Locate and identify every blood parasite.
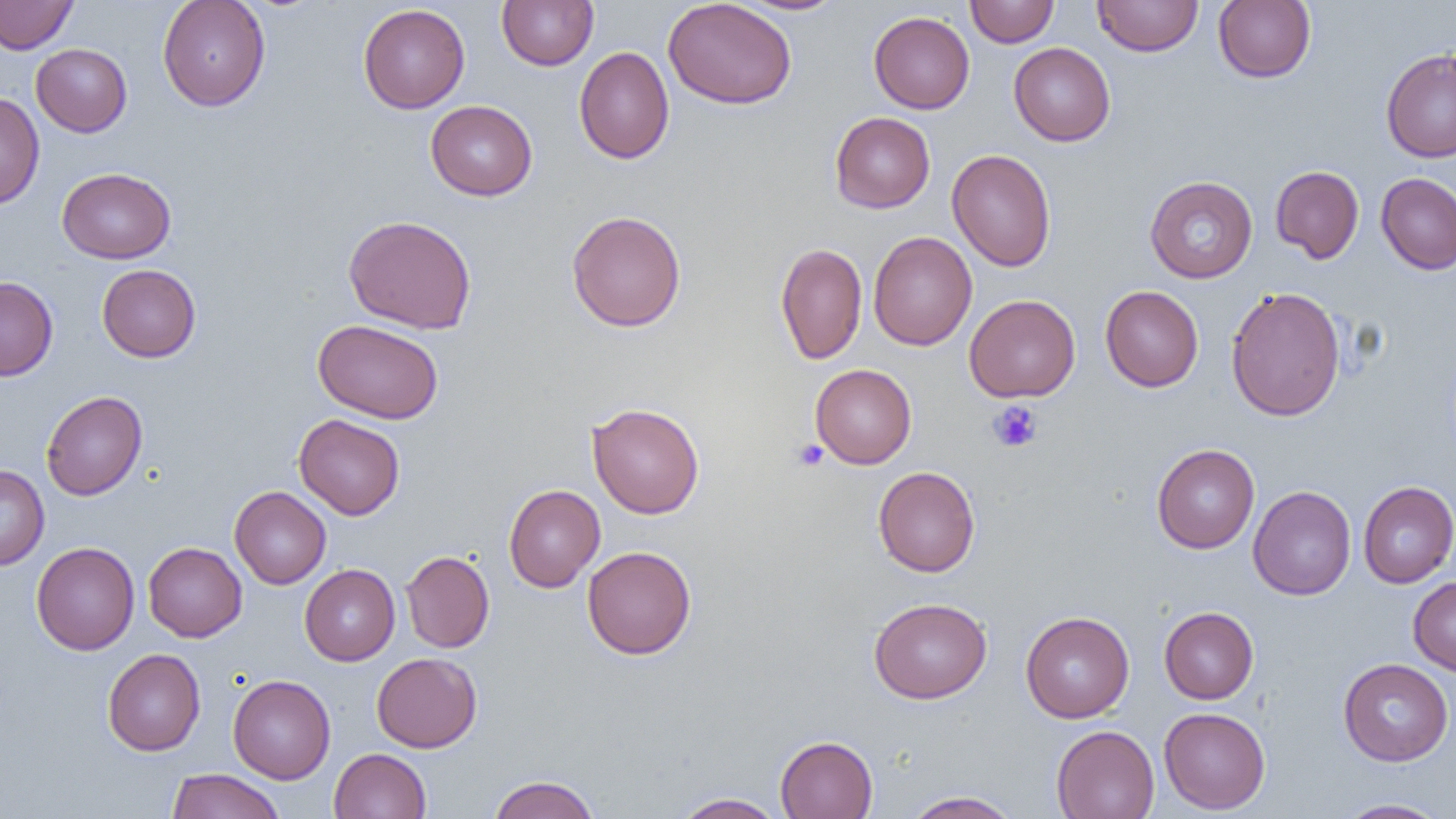
No blood parasites observed.

Summary:
  - Coordinate format: approximate bounding boxes as [x1, y1, x2, y2] in pixels
  - Platelet locations: [987, 401, 1043, 452], [793, 439, 829, 471]
  - Uninfected red blood cell locations: [0, 0, 78, 54], [157, 0, 271, 111], [497, 0, 599, 70], [663, 0, 797, 109], [736, 0, 849, 15], [965, 0, 1058, 47], [1092, 0, 1202, 57], [1213, 0, 1316, 83], [358, 3, 470, 114], [868, 11, 974, 114], [1008, 42, 1115, 146], [31, 44, 132, 137], [574, 46, 674, 164], [1381, 48, 1456, 163], [0, 91, 45, 209], [425, 100, 537, 201], [830, 112, 935, 213], [947, 149, 1056, 272], [1270, 165, 1364, 263], [57, 167, 175, 264], [1376, 172, 1456, 275], [1144, 176, 1258, 283], [566, 210, 686, 332], [343, 214, 477, 334], [868, 231, 976, 351], [775, 242, 868, 365], [96, 264, 201, 362], [0, 276, 58, 381], [1100, 285, 1203, 392], [1225, 286, 1346, 422], [964, 294, 1081, 402], [313, 319, 444, 424], [810, 364, 917, 469], [41, 391, 147, 500], [586, 402, 704, 519], [294, 414, 405, 520], [1151, 443, 1259, 553], [0, 464, 49, 570], [873, 466, 980, 577], [1358, 481, 1456, 588], [503, 484, 605, 592], [1248, 485, 1356, 600], [229, 486, 331, 589], [31, 541, 139, 655], [143, 542, 247, 642], [582, 545, 696, 659], [401, 550, 494, 652], [299, 564, 400, 666], [1408, 576, 1456, 676], [868, 597, 992, 704], [1159, 606, 1258, 703], [1020, 611, 1134, 722], [102, 648, 205, 756], [371, 652, 482, 752], [1338, 658, 1454, 766], [228, 674, 336, 784], [1159, 707, 1270, 813], [1051, 725, 1159, 818], [775, 735, 877, 818], [329, 748, 431, 819], [165, 768, 285, 819], [488, 774, 600, 819], [903, 790, 1022, 818], [673, 792, 786, 819], [1334, 799, 1449, 818]
  - Slide-level diagnosis: negative for blood parasites
  - Image size: 1456×819 pixels
  - Field of view: single
  - Modality: optical microscopy
  - Preparation: thin blood smear
  - Magnification: 1000x